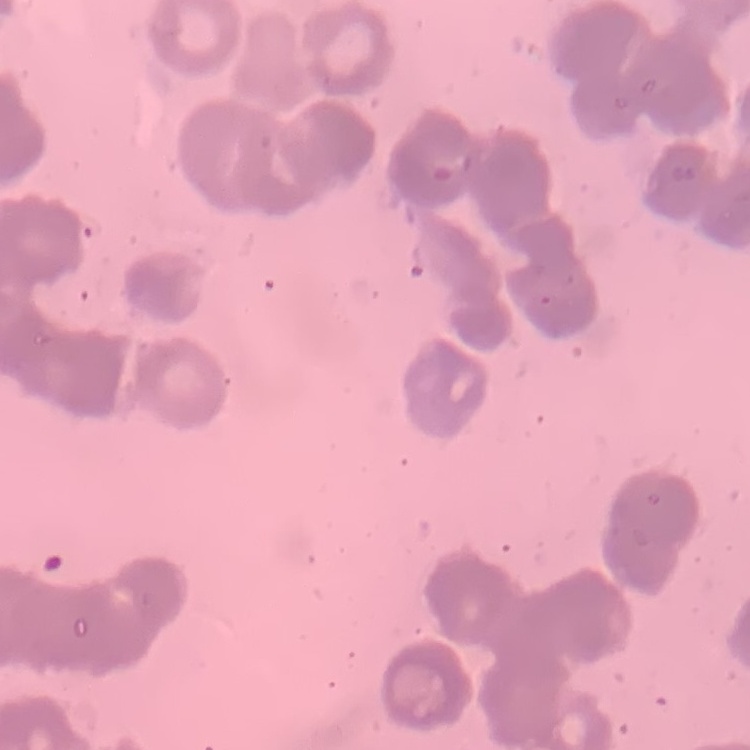
The erythrocytes show rouleaux formation. Thin peripheral smear. Stained with either Field's or Giemsa. One tile cut from a larger photomicrograph.